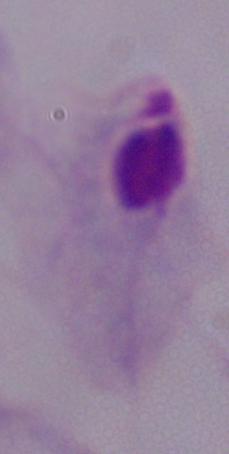

Summary:
  - Identification: trichomonad
  - Modality: photomicrograph
  - Magnification: 1000x